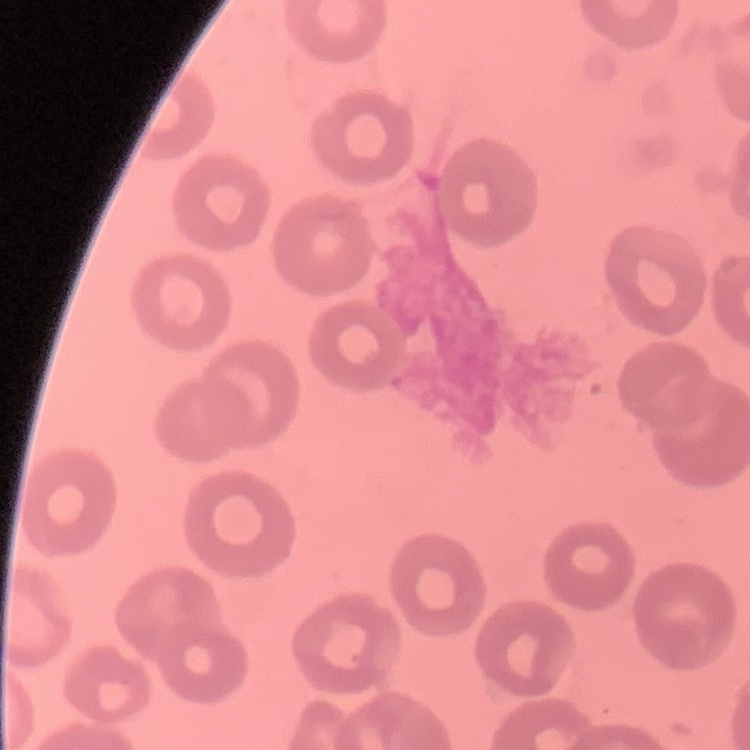

erythrocyte morphology = no rouleaux formation
preparation = thin peripheral smear
image type = one tile cut from a larger photomicrograph
stain = Field's or Giemsa